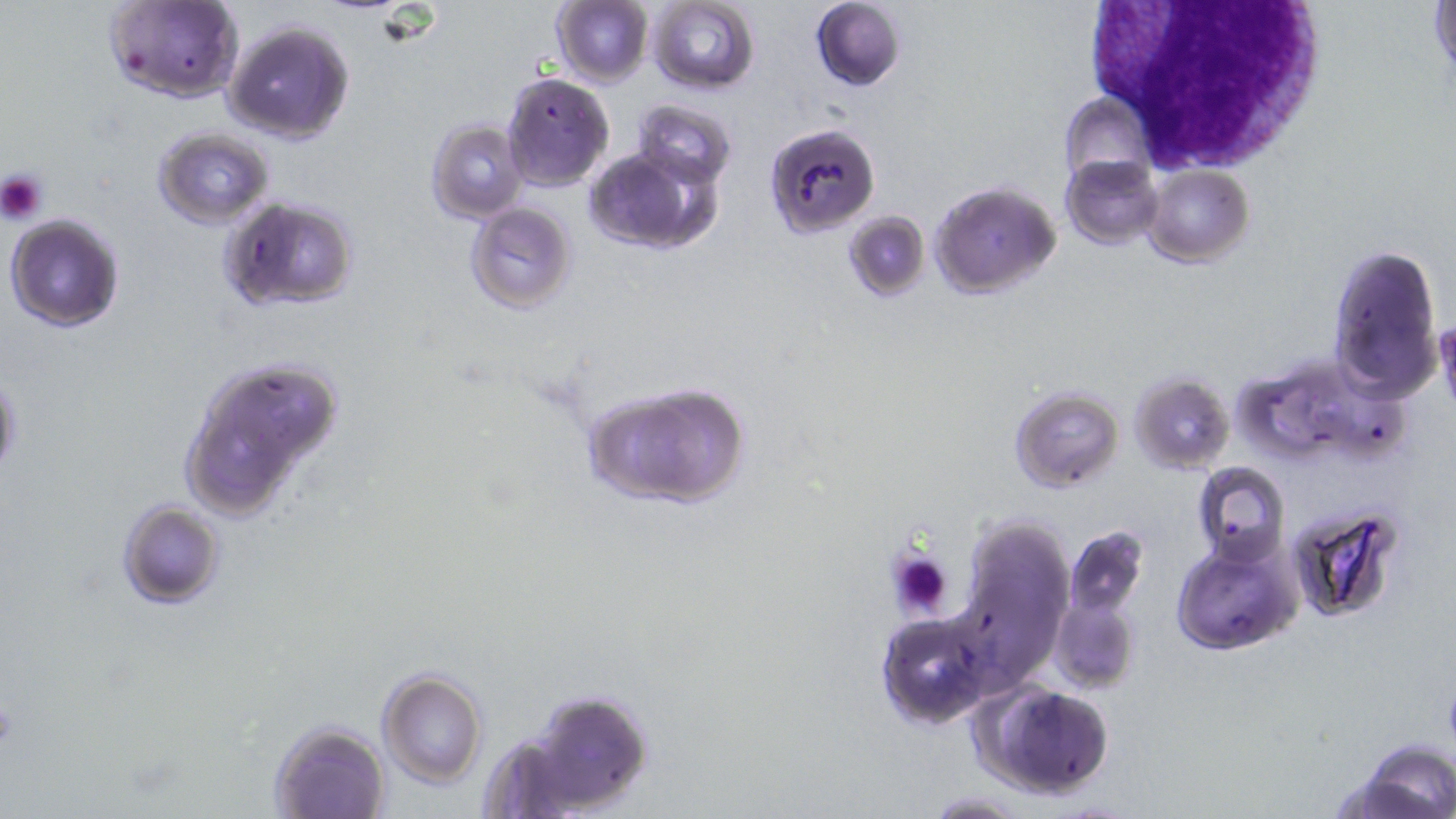
Summary:
  - Coordinate format: approximate bounding boxes as (x1, y1, x2, y2) in pixels
  - Platelet locations: (0, 169, 49, 224), (888, 549, 953, 619), (0, 697, 18, 751)
  - White blood cell locations: (1078, 2, 1332, 173)
  - Uninfected red blood cell locations: (103, 0, 244, 104), (809, 0, 906, 90), (549, 1, 653, 87), (645, 2, 760, 93), (1428, 2, 1455, 88), (224, 19, 357, 145), (502, 73, 614, 190), (1060, 91, 1154, 184), (631, 98, 738, 188), (425, 118, 528, 223), (766, 122, 880, 238), (151, 127, 276, 230), (584, 148, 713, 255), (1062, 155, 1165, 250), (1141, 165, 1252, 267), (930, 180, 1060, 299), (218, 197, 359, 313), (464, 202, 576, 312), (844, 210, 931, 299), (5, 213, 127, 333), (1328, 241, 1442, 403), (1231, 348, 1407, 471), (174, 352, 349, 522), (0, 369, 23, 485), (1130, 373, 1233, 476), (583, 381, 751, 510), (1009, 386, 1124, 492), (1192, 462, 1289, 566), (117, 500, 224, 608), (1287, 506, 1407, 625), (956, 513, 1075, 664), (1063, 524, 1149, 635), (1173, 534, 1302, 656), (1048, 581, 1140, 696), (875, 613, 992, 728), (376, 670, 487, 787), (972, 680, 1118, 800), (525, 689, 653, 813), (269, 718, 390, 819), (1345, 740, 1456, 819), (921, 791, 1034, 818)
  - Slide-level diagnosis: Plasmodium falciparum
  - Image size: 1456×819 pixels
  - Field of view: single
  - Stain: May-Grünwald-Giemsa
  - Magnification: 1000x
  - Modality: light microscopy
  - Preparation: thin blood film